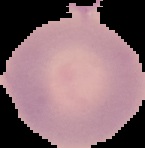
Summary:
  - Result: no Plasmodium parasites detected
  - Preparation: thin blood smear
  - Image size: 145×148 pixels
  - Image type: cell region segmented out of the field of view; surrounding area masked to black